Assess this cell for malaria.
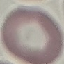

Uninfected.

Photographed with a smartphone camera at the microscope eyepiece. Automatically extracted cell patch, resized to 64 × 64 pixels. Thin blood smear. Giemsa-stained preparation.